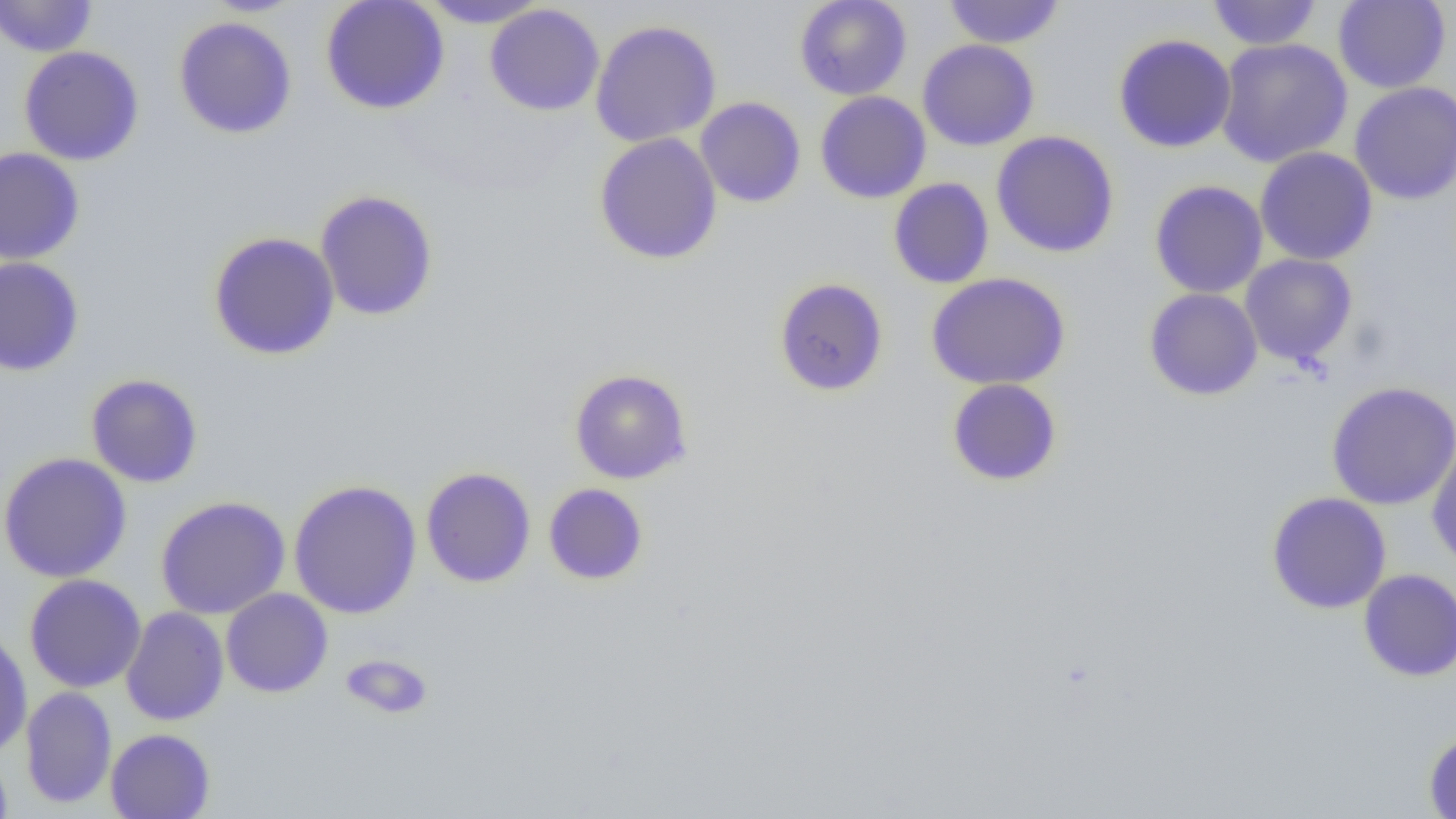
Summary:
  - Coordinate format: approximate bounding boxes as [x1, y1, x2, y2] in pixels
  - Uninfected red blood cell locations: [0, 0, 98, 57], [320, 0, 450, 115], [418, 0, 550, 29], [794, 0, 911, 100], [942, 0, 1066, 49], [1206, 0, 1322, 50], [1333, 0, 1450, 93], [485, 4, 604, 116], [173, 15, 297, 139], [590, 19, 722, 147], [1113, 33, 1237, 153], [1215, 37, 1353, 168], [917, 39, 1040, 151], [18, 46, 145, 166], [1350, 81, 1456, 205], [815, 91, 931, 204], [695, 97, 806, 208], [991, 130, 1120, 258], [593, 133, 723, 265], [0, 147, 85, 264], [1255, 147, 1377, 266], [888, 178, 994, 289], [1150, 179, 1268, 298], [314, 189, 439, 321], [208, 231, 340, 360], [1240, 254, 1357, 367], [0, 257, 84, 376], [926, 272, 1070, 390], [773, 277, 889, 396], [1143, 287, 1263, 401], [569, 368, 693, 484], [86, 373, 203, 488], [946, 378, 1063, 486], [1326, 381, 1456, 510], [1426, 437, 1456, 572], [0, 452, 132, 583], [421, 467, 536, 588], [288, 479, 422, 619], [543, 483, 649, 585], [1266, 492, 1392, 614], [155, 496, 290, 619], [1359, 568, 1456, 681], [24, 574, 147, 693], [221, 588, 333, 697], [121, 606, 229, 725], [0, 627, 33, 759], [340, 653, 434, 719], [20, 687, 117, 808], [105, 728, 215, 819], [1423, 730, 1456, 819], [0, 745, 13, 819]
  - Slide-level diagnosis: no evidence of blood parasites
  - Modality: optical microscopy
  - Magnification: 1000x
  - Field of view: single
  - Image size: 1456×819 pixels
  - Preparation: thin blood film